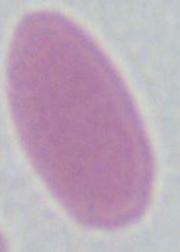
identification: erythrocyte
modality: photomicrograph
magnification: 1000x